Comment on the morphology of the red blood cells.
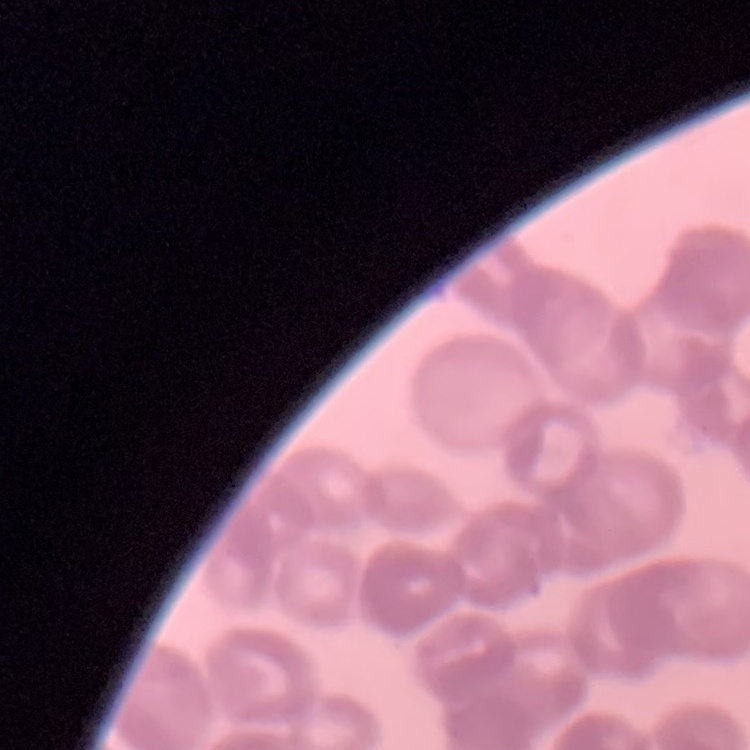
Rouleaux formation.

Square crop of a larger photomicrograph. Field's or Giemsa stain. Thin peripheral smear.